Report the malaria status of this cell.
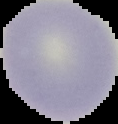
Uninfected.

Image is 118×124 pixels. Segmented cell region on a black background. From a thin blood smear.